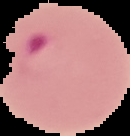
Result: Plasmodium parasites detected. From a thin blood film. Image is 130×136 pixels. Cell region segmented out of the field of view; the surrounding area is masked to black.